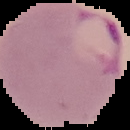

Summary:
  - Image type: cell region segmented out of the field of view; surrounding area masked to black
  - Malaria status: parasitized
  - Image size: 130×130 pixels
  - Preparation: thin blood film